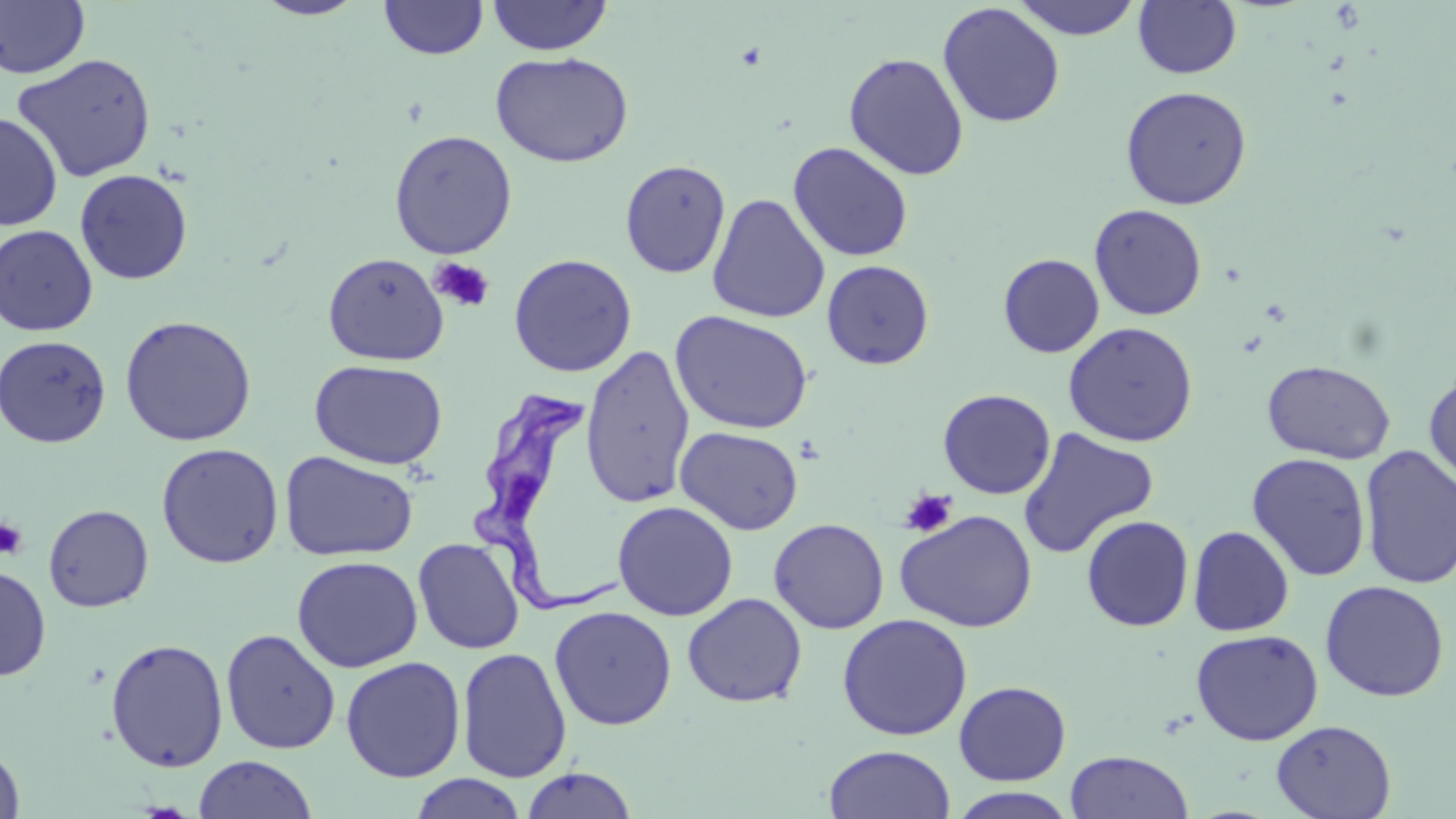
Summary:
  - Coordinate format: approximate bounding boxes as named x1/y1/x2/y2 corners in pixels
  - Trypanosoma brucei locations: (x1=465, y1=389, x2=622, y2=619)
  - Uninfected red blood cell locations: (x1=251, y1=0, x2=369, y2=20), (x1=379, y1=0, x2=488, y2=60), (x1=487, y1=0, x2=613, y2=56), (x1=1012, y1=0, x2=1142, y2=40), (x1=0, y1=1, x2=91, y2=79), (x1=1133, y1=1, x2=1242, y2=79), (x1=937, y1=3, x2=1065, y2=128), (x1=490, y1=51, x2=634, y2=168), (x1=843, y1=52, x2=969, y2=180), (x1=12, y1=53, x2=157, y2=183), (x1=1120, y1=85, x2=1252, y2=210), (x1=0, y1=112, x2=62, y2=231), (x1=389, y1=130, x2=518, y2=259), (x1=788, y1=142, x2=914, y2=262), (x1=620, y1=159, x2=732, y2=278), (x1=74, y1=169, x2=193, y2=285), (x1=707, y1=194, x2=830, y2=323), (x1=1089, y1=204, x2=1207, y2=321), (x1=0, y1=224, x2=98, y2=336), (x1=322, y1=252, x2=449, y2=366), (x1=508, y1=253, x2=637, y2=377), (x1=998, y1=253, x2=1104, y2=358), (x1=821, y1=259, x2=934, y2=369), (x1=671, y1=310, x2=814, y2=435), (x1=119, y1=315, x2=257, y2=446), (x1=1063, y1=321, x2=1199, y2=447), (x1=0, y1=335, x2=112, y2=448), (x1=580, y1=344, x2=695, y2=508), (x1=309, y1=359, x2=448, y2=470), (x1=1261, y1=360, x2=1396, y2=464), (x1=1424, y1=368, x2=1456, y2=495), (x1=937, y1=389, x2=1056, y2=499), (x1=675, y1=426, x2=804, y2=535), (x1=1017, y1=427, x2=1159, y2=560), (x1=156, y1=442, x2=284, y2=568), (x1=1359, y1=445, x2=1456, y2=589), (x1=279, y1=451, x2=418, y2=561), (x1=1247, y1=452, x2=1371, y2=581), (x1=612, y1=501, x2=738, y2=621), (x1=43, y1=504, x2=153, y2=612), (x1=895, y1=509, x2=1037, y2=633), (x1=1080, y1=515, x2=1194, y2=632), (x1=768, y1=518, x2=889, y2=634), (x1=1188, y1=525, x2=1295, y2=636), (x1=413, y1=537, x2=525, y2=654), (x1=292, y1=555, x2=423, y2=673), (x1=0, y1=565, x2=51, y2=681), (x1=1320, y1=579, x2=1450, y2=702), (x1=682, y1=593, x2=807, y2=707), (x1=549, y1=605, x2=677, y2=730), (x1=837, y1=613, x2=973, y2=741), (x1=221, y1=628, x2=340, y2=755), (x1=1190, y1=629, x2=1324, y2=746), (x1=105, y1=638, x2=229, y2=772), (x1=457, y1=647, x2=572, y2=783), (x1=341, y1=656, x2=465, y2=783), (x1=953, y1=680, x2=1071, y2=785), (x1=1271, y1=720, x2=1397, y2=818), (x1=0, y1=740, x2=26, y2=819), (x1=823, y1=744, x2=956, y2=819), (x1=1065, y1=750, x2=1193, y2=818), (x1=193, y1=755, x2=317, y2=818), (x1=520, y1=766, x2=638, y2=818), (x1=410, y1=773, x2=527, y2=819), (x1=947, y1=786, x2=1079, y2=819)
  - Platelet locations: (x1=429, y1=257, x2=495, y2=313), (x1=900, y1=488, x2=957, y2=537), (x1=0, y1=517, x2=28, y2=559)
  - Slide-level diagnosis: Trypanosoma brucei
  - Field of view: one of a larger specimen
  - Stain: May-Grünwald-Giemsa
  - Modality: optical microscopy
  - Magnification: 1000x
  - Preparation: thin blood film
  - Image size: 1456×819 pixels